Outline each uninfected red blood cell.
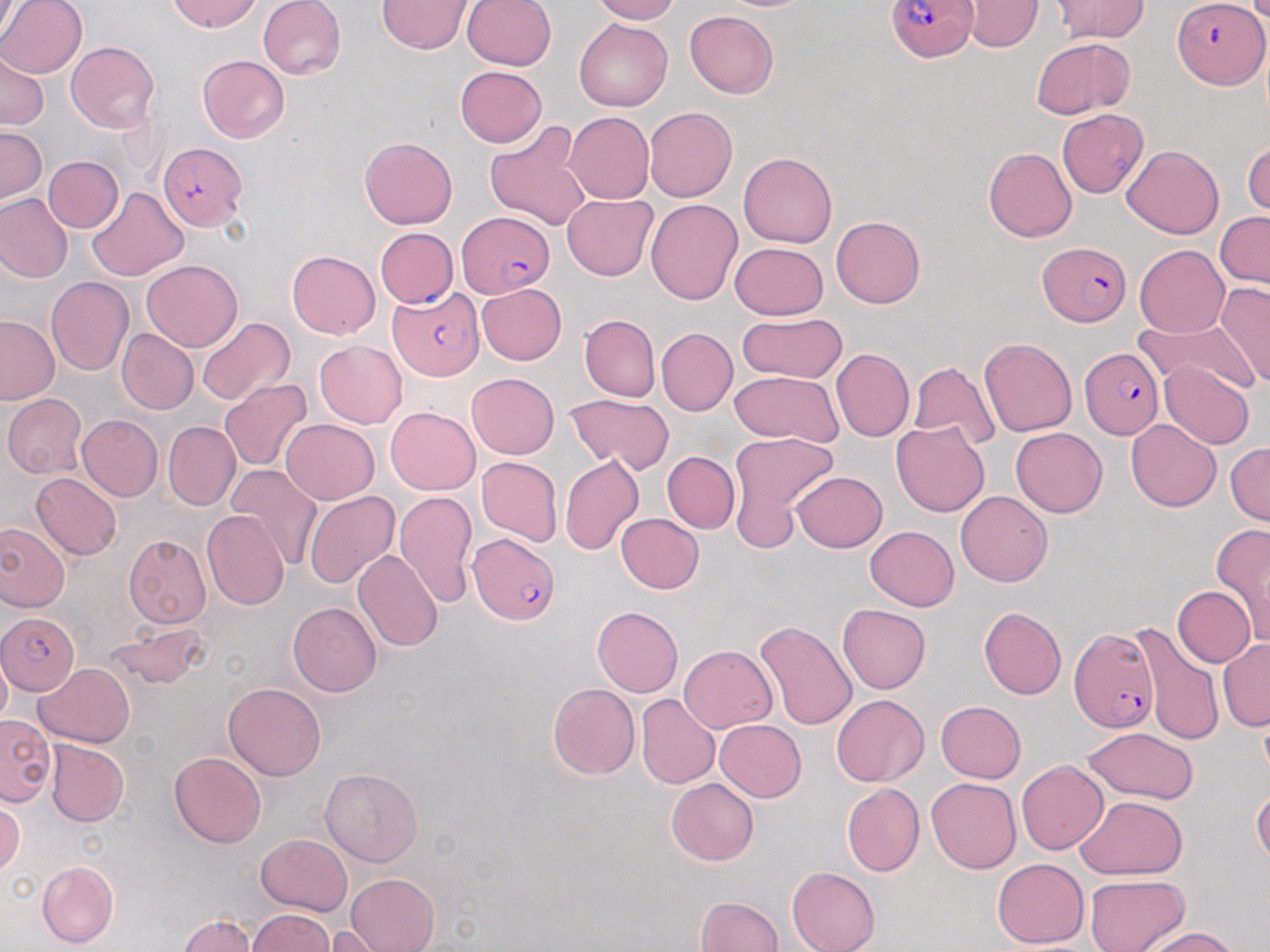
Approximate bounding boxes as (x1,y1)-(x2,y2) corner pairs in pixels.
Uninfected red blood cells: (0,0)-(87,79), (0,0)-(21,46), (169,0)-(261,32), (258,0)-(347,79), (590,0)-(679,24), (965,0)-(1041,52), (377,1)-(474,54), (462,1)-(555,71), (1052,1)-(1149,42), (1246,1)-(1270,22), (685,10)-(779,99), (574,18)-(672,111), (1032,37)-(1133,119), (66,41)-(160,134), (0,52)-(48,131), (198,55)-(289,142), (454,66)-(547,147), (464,71)-(572,198), (644,107)-(737,202), (1057,110)-(1149,198), (564,112)-(653,204), (485,122)-(592,232), (0,126)-(46,203), (360,137)-(456,229), (1243,140)-(1270,217), (1121,145)-(1224,239), (983,147)-(1077,242), (738,152)-(837,248), (44,156)-(123,232), (86,187)-(187,281), (0,193)-(73,283), (561,194)-(657,280), (645,197)-(743,305), (1215,212)-(1270,289), (830,216)-(925,308), (375,227)-(458,307), (729,242)-(828,320), (1134,243)-(1229,337), (287,250)-(380,339), (141,260)-(242,351), (45,276)-(133,375), (476,283)-(566,366), (1215,283)-(1270,389), (736,313)-(847,384), (579,315)-(660,402), (0,316)-(59,406), (197,317)-(295,405), (1134,317)-(1255,394), (656,328)-(737,416), (116,329)-(197,414), (979,337)-(1077,436), (313,341)-(408,428), (830,348)-(914,442), (1158,360)-(1255,450), (909,362)-(1001,451), (728,371)-(845,446), (466,373)-(559,460), (219,379)-(310,471), (1,393)-(87,479), (564,394)-(674,473), (385,406)-(480,494), (76,414)-(162,502), (281,419)-(379,504), (1125,419)-(1221,512), (163,422)-(240,509), (891,422)-(990,517), (1011,428)-(1106,517), (728,432)-(839,541), (1225,443)-(1270,523), (663,451)-(739,533), (560,454)-(644,556), (476,457)-(562,547), (225,464)-(322,567), (792,471)-(886,552), (30,472)-(122,560), (6,482)-(110,599), (956,490)-(1052,586), (303,491)-(400,588), (394,491)-(477,607), (202,511)-(290,611), (615,513)-(704,594), (0,521)-(70,613), (1212,523)-(1270,641), (864,525)-(958,611), (123,534)-(211,628), (353,550)-(443,652), (1172,585)-(1255,667), (288,602)-(382,697), (837,603)-(931,694), (592,606)-(682,697), (978,607)-(1065,700), (755,620)-(858,732), (104,621)-(209,690), (1131,623)-(1224,747), (1218,639)-(1269,731), (678,645)-(777,733), (0,651)-(11,730), (35,663)-(135,748), (223,682)-(326,781), (547,684)-(639,780), (635,692)-(720,789), (832,694)-(929,786), (934,701)-(1026,783), (0,713)-(55,805), (714,719)-(806,801), (1081,726)-(1199,805), (45,740)-(128,826), (169,751)-(266,848), (1016,760)-(1109,855), (320,767)-(422,866), (666,778)-(758,866), (926,778)-(1021,873), (842,784)-(924,876), (1251,785)-(1270,868), (1076,795)-(1187,879), (0,798)-(24,875), (256,834)-(352,916), (991,857)-(1090,948), (36,860)-(119,948), (787,867)-(879,952), (345,873)-(440,952), (1083,874)-(1190,952), (695,896)-(782,951), (247,909)-(334,951), (180,914)-(257,952), (318,925)-(401,951), (1137,926)-(1237,952).

slide_level_diagnosis: Plasmodium falciparum
preparation: thin blood smear
field_of_view: one of a larger specimen
modality: optical microscopy
plasmodium_falciparum_infected_red_blood_cell_locations: 'approximate bounding boxes as (x1,y1)-(x2,y2) corner pairs in pixels: (888,0)-(977,62), (1174,1)-(1268,89), (157,141)-(246,228), (456,214)-(553,297), (1040,241)-(1131,326), (388,290)-(482,380), (1080,347)-(1162,439), (466,534)-(560,626), (0,612)-(78,694), (1068,627)-(1159,734)'
stain: May-Grünwald-Giemsa
image_size: 1270×952 pixels
magnification: 1000x